Identify the preparation type.
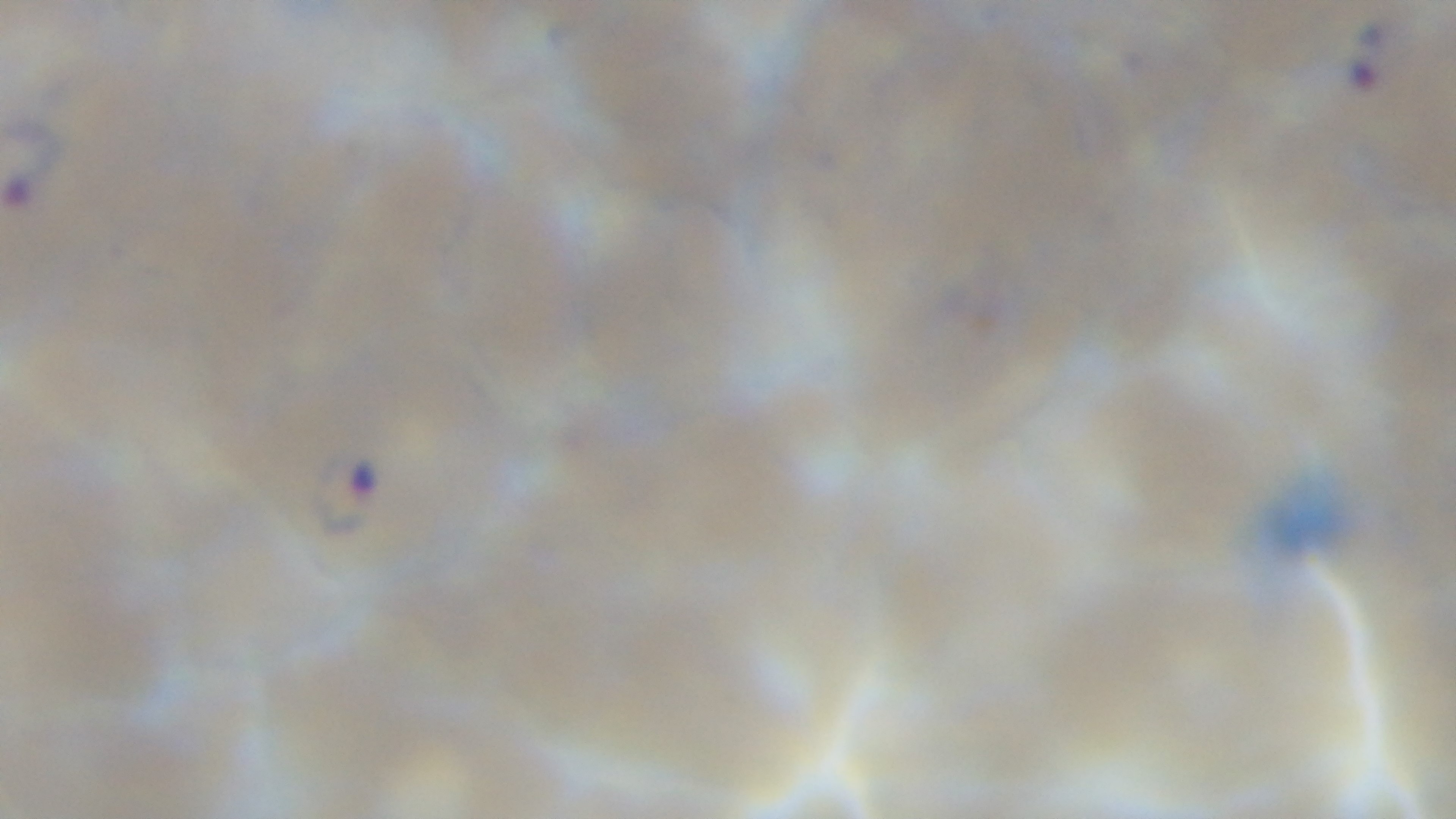

Thin.

malaria status = infected
stain = Giemsa
capture = mounted 4K digital camera
field of view = single
objective = 100x oil immersion
modality = light microscopy